Identify the blood parasite species.
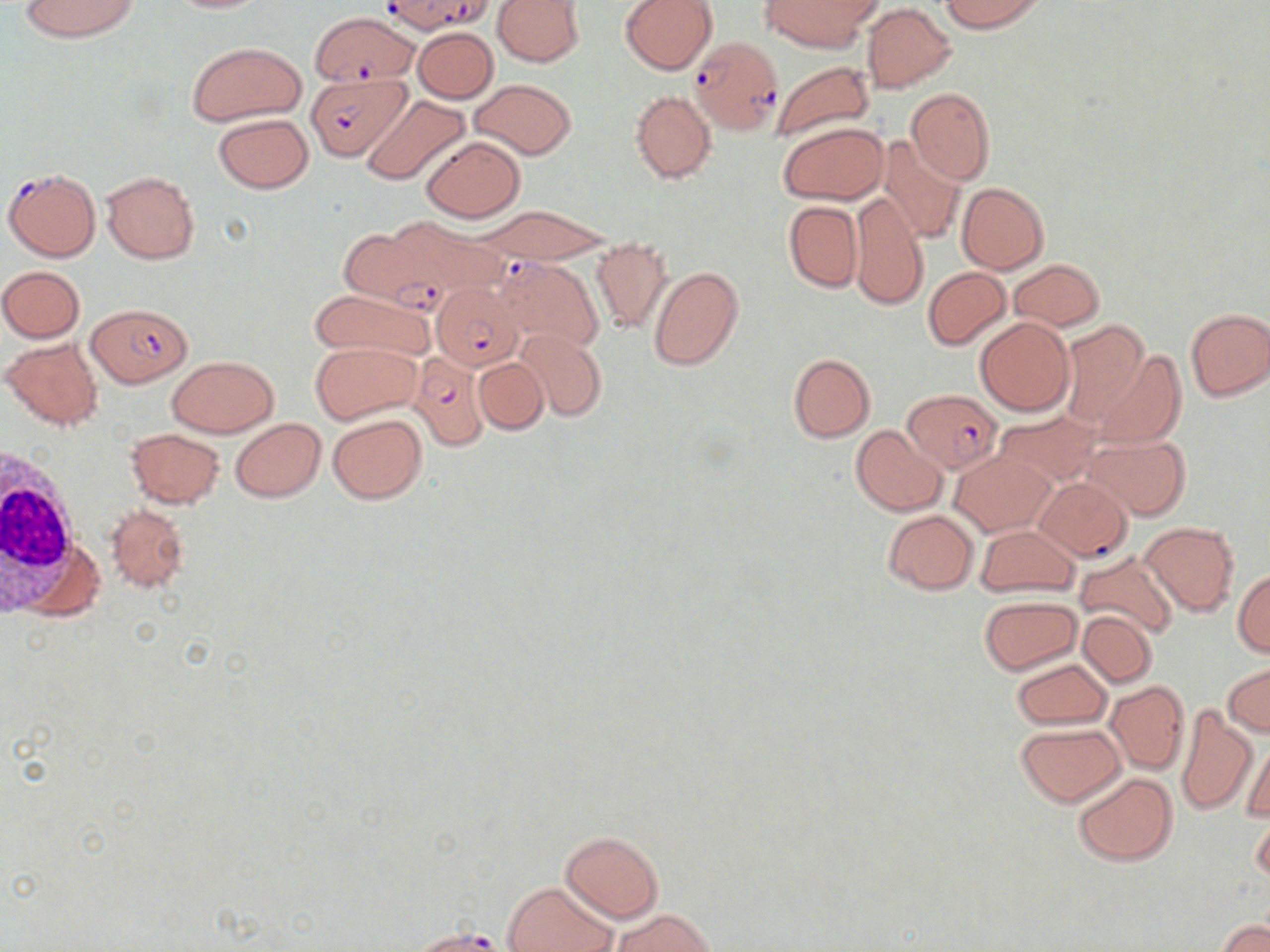
Plasmodium falciparum.

Approximate bounding boxes as (x1,y1)-(x2,y2) corner pairs in pixels. Plasmodium falciparum-infected red blood cell locations: (379,0)-(492,35), (311,12)-(420,86), (690,37)-(783,134), (306,69)-(408,162), (3,167)-(101,262), (352,218)-(479,310), (495,256)-(604,356), (432,282)-(525,369), (87,304)-(192,387), (410,353)-(491,451), (903,389)-(1002,474), (407,927)-(508,951). White blood cell locations: (0,453)-(90,616). Uninfected red blood cell locations: (19,0)-(141,43), (161,0)-(272,13), (492,0)-(587,68), (620,0)-(716,74), (760,0)-(873,53), (938,0)-(1046,32), (861,4)-(956,92), (413,26)-(498,102), (186,41)-(305,126), (769,59)-(875,147), (470,79)-(577,159), (906,87)-(996,186), (630,89)-(715,184), (360,94)-(470,185), (213,113)-(313,193), (779,122)-(887,204), (420,135)-(525,222), (879,135)-(967,246), (101,171)-(199,264), (956,182)-(1049,274), (848,194)-(928,311), (783,202)-(862,292), (472,207)-(615,263), (590,240)-(673,334), (1009,259)-(1103,331), (0,265)-(86,342), (648,266)-(743,372), (923,267)-(1011,350), (309,288)-(434,363), (1184,307)-(1270,401), (975,316)-(1073,416), (1058,319)-(1149,427), (515,329)-(608,421), (2,336)-(104,430), (312,341)-(419,422), (1092,349)-(1186,448), (788,353)-(875,442), (168,356)-(277,436), (473,357)-(548,434), (994,410)-(1101,490), (328,412)-(426,504), (231,418)-(326,502), (851,425)-(947,516), (126,427)-(226,508), (1084,434)-(1191,520), (953,451)-(1055,535), (1036,476)-(1133,561), (105,504)-(189,593), (882,510)-(979,593), (1139,523)-(1239,615), (975,524)-(1080,597), (1074,551)-(1178,641), (1232,569)-(1270,657), (980,596)-(1082,674), (1077,609)-(1156,687), (1010,657)-(1110,730), (1224,664)-(1270,736), (1106,681)-(1189,773), (1174,702)-(1257,817), (1016,724)-(1125,805), (1241,736)-(1269,825), (1073,772)-(1176,866), (1251,805)-(1270,888), (561,830)-(663,923), (503,881)-(616,952), (611,909)-(715,952), (1219,919)-(1268,952). Single field of view. Thin blood smear. Captured at 1000x magnification. Image is 1270×952 pixels. May-Grünwald-Giemsa stain. Light microscopy.